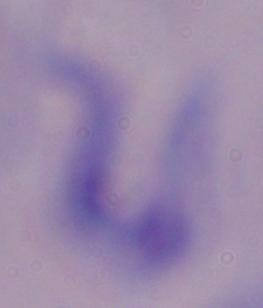

Summary:
  - Identification: trypanosome
  - Magnification: 1000x
  - Modality: micrograph